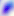

magnification: 400x
identification: Toxoplasma gondii
modality: micrograph